Locate every leukocyte (white blood cell).
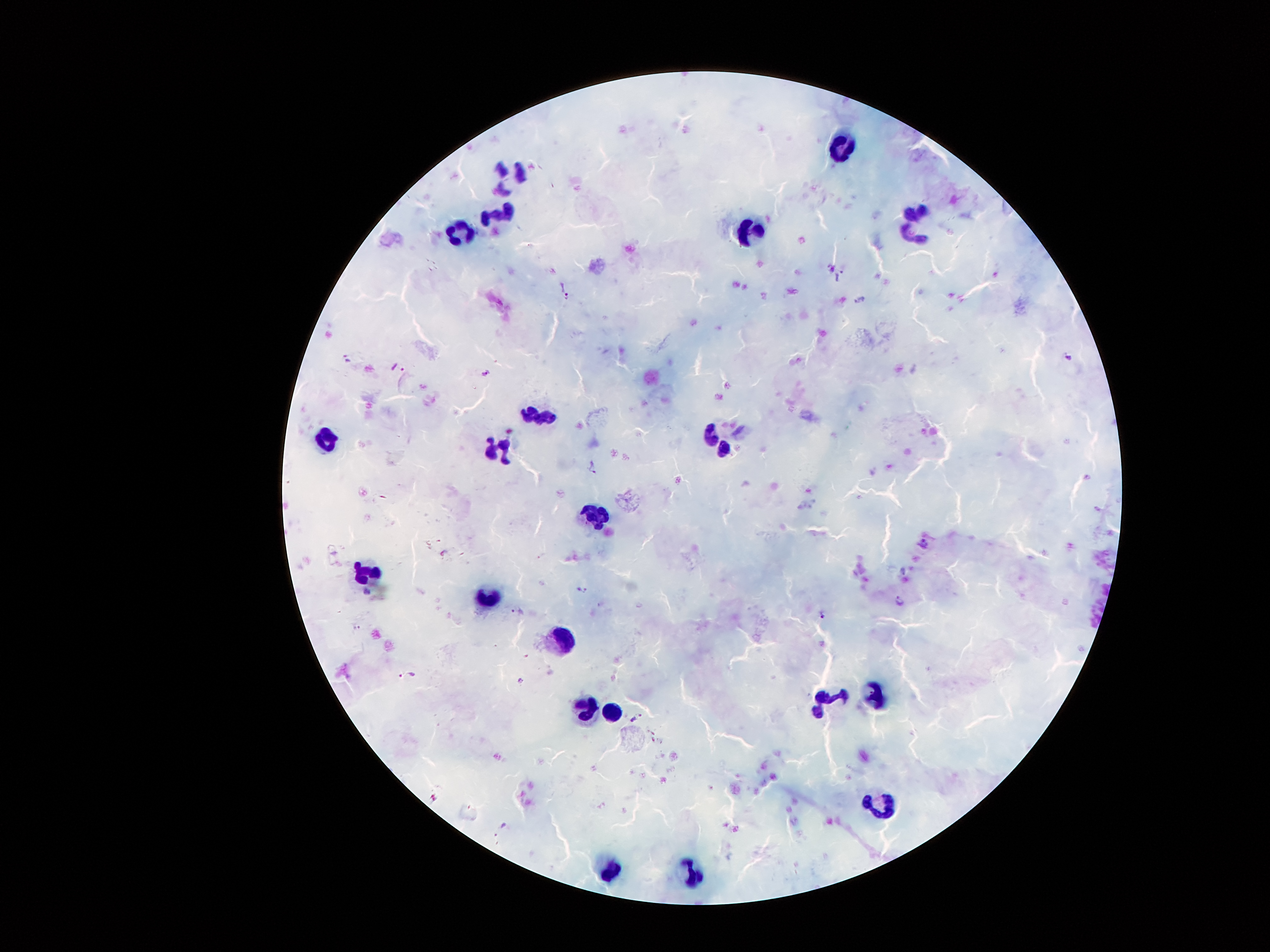

Approximate centers as {x, y} in pixels.
Leukocytes: {840, 144}, {509, 170}, {914, 218}, {494, 221}, {749, 228}, {455, 236}, {538, 412}, {722, 441}, {323, 442}, {499, 450}, {596, 513}, {370, 580}, {493, 597}, {559, 642}, {874, 694}, {829, 699}, {588, 707}, {614, 712}, {882, 815}, {611, 870}, {686, 872}.

{
  "field_of_view": "single",
  "magnification": "100x",
  "patient_malaria_status": "infected with Plasmodium falciparum",
  "capture": "smartphone camera through the microscope eyepiece",
  "stain": "Giemsa",
  "plasmodium_parasite_locations": "approximate centers as {x, y} in pixels: {842, 268}, {567, 296}, {862, 301}, {1069, 357}, {348, 359}, {403, 369}, {485, 373}, {925, 545}, {584, 591}, {900, 601}, {822, 615}, {635, 720}",
  "image_size": "1270×952 pixels",
  "preparation": "thick peripheral-blood smear"
}